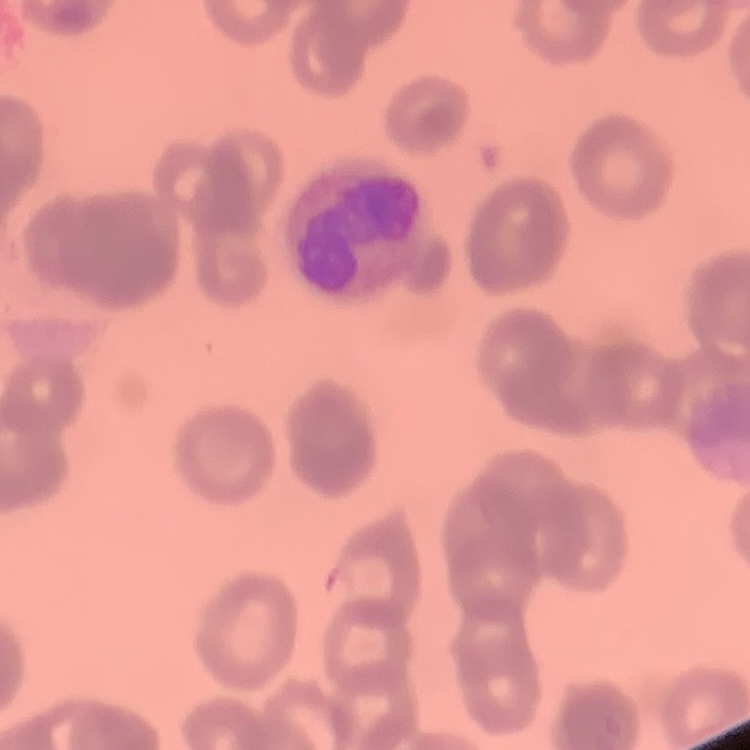

erythrocyte morphology = rouleaux formation
stain = Field's or Giemsa
image type = square crop of a larger photomicrograph
preparation = thin blood film